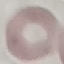

Summary:
  - Malaria status: uninfected
  - Stain: Giemsa
  - Capture: smartphone through the microscope eyepiece
  - Preparation: thin blood smear
  - Image type: cell patch, automatically extracted from a larger field of view and resized to 64 × 64 pixels